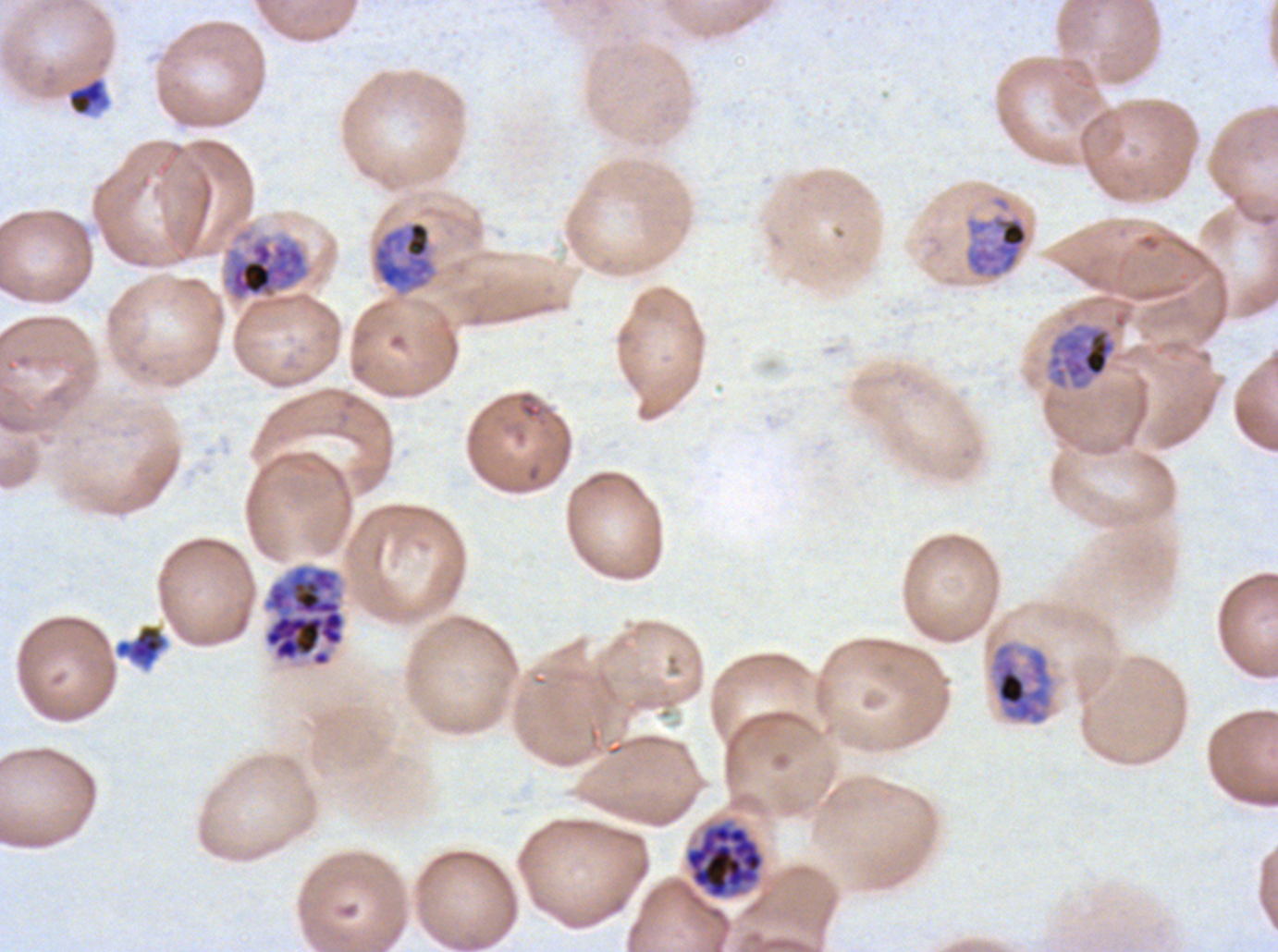
{
  "field_of_view": "one sub-image of a larger composite",
  "debris_locations": "approximate bounding boxes as [x1, y1, x2, y2] in pixels: [67, 77, 110, 116], [115, 624, 167, 668]",
  "late_trophozoite_locations": "approximate bounding boxes as [x1, y1, x2, y2] in pixels: [964, 212, 1029, 279], [372, 220, 436, 291], [1046, 322, 1117, 391]",
  "specimen": "ex-vivo Plasmodium falciparum culture from a patient in The Gambia, grown for 24 to 48 hours",
  "early_schizont_locations": "approximate bounding boxes as [x1, y1, x2, y2] in pixels: [220, 228, 312, 303], [988, 640, 1055, 726]",
  "preparation": "thin blood film",
  "stain": "Giemsa",
  "life_cycle_stages_observed": "late trophozoite, early schizont, segmenter",
  "image_size": "1278×952 pixels",
  "segmenter_locations": "approximate bounding boxes as [x1, y1, x2, y2] in pixels: [262, 562, 347, 668], [684, 822, 765, 899]"
}